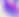
Captured at 400x magnification. Toxoplasma gondii is shown. Micrograph.